Give the position of every Plasmodium parasite.
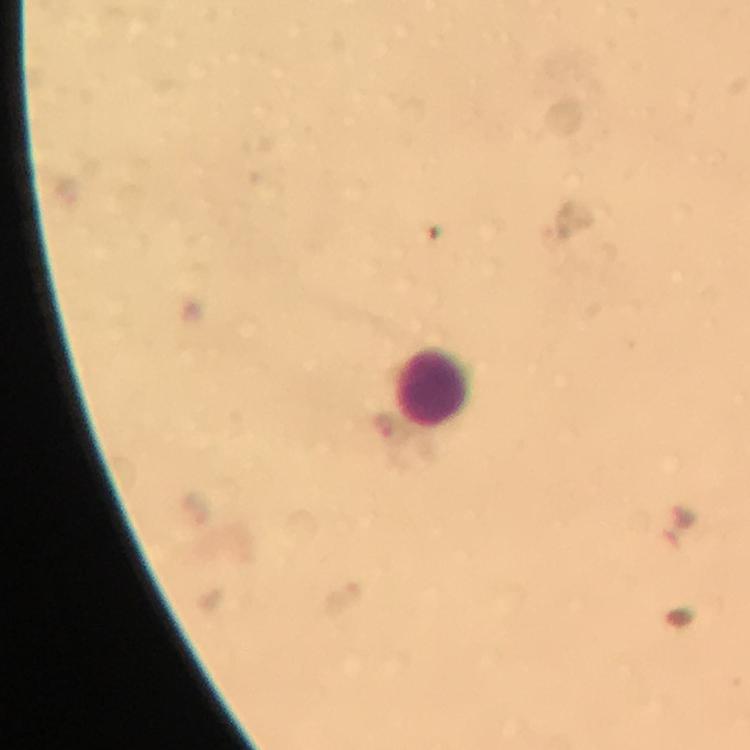

Approximate centers as {x, y} in pixels.
Plasmodium parasites: {385, 431}, {343, 599}.

Summary:
  - Leukocyte locations: {434, 388}
  - Image size: 750×750 pixels
  - Capture: smartphone camera through the microscope
  - Stain: Giemsa
  - Cropped from: one field of view
  - Context: from a diagnostic examination for malaria
  - Preparation: thick blood film
  - Immersion oil: applied
  - Magnification: 100x